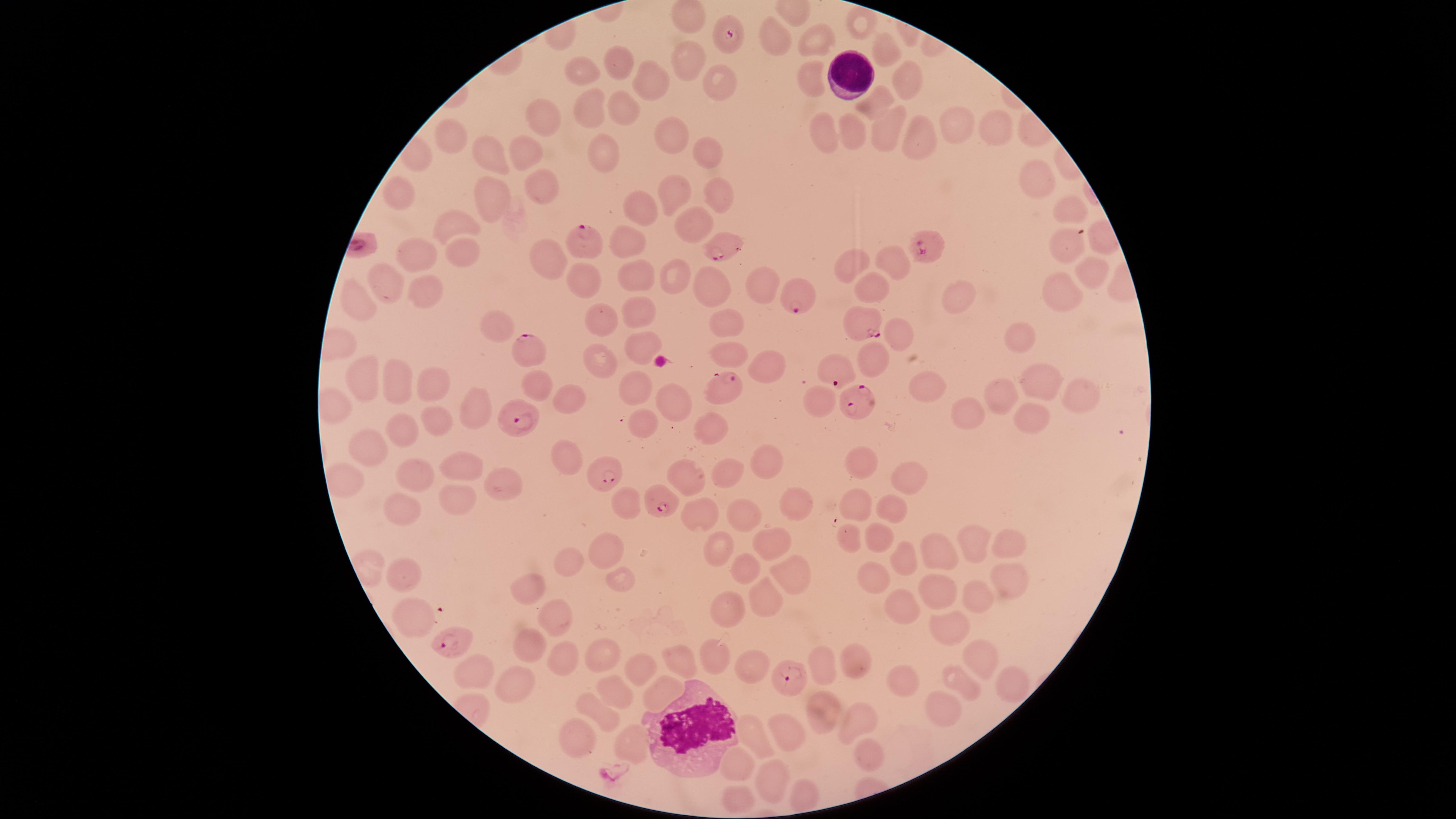
visible region = circular
preparation = thin smear of blood
species = Plasmodium falciparum
uninfected RBCs = approximate marker points, in pixels from the top-left corner: (x=862, y=21), (x=773, y=35), (x=810, y=36), (x=885, y=47), (x=687, y=52), (x=617, y=64), (x=586, y=73), (x=904, y=76), (x=810, y=79), (x=715, y=81), (x=655, y=84), (x=881, y=101), (x=620, y=106), (x=587, y=110), (x=541, y=122), (x=957, y=122), (x=885, y=124), (x=992, y=127), (x=915, y=132), (x=822, y=133), (x=854, y=134), (x=452, y=136), (x=673, y=137), (x=704, y=149), (x=494, y=153), (x=527, y=155), (x=602, y=158), (x=1033, y=178), (x=541, y=182), (x=677, y=189), (x=722, y=191), (x=399, y=197), (x=492, y=197), (x=640, y=209), (x=1068, y=209), (x=696, y=222), (x=449, y=224), (x=629, y=242), (x=1067, y=243), (x=459, y=256), (x=414, y=258), (x=891, y=260), (x=543, y=265), (x=850, y=267), (x=1091, y=272), (x=584, y=276), (x=636, y=277), (x=675, y=277), (x=707, y=285), (x=388, y=287), (x=759, y=287), (x=876, y=289), (x=1064, y=290), (x=427, y=293), (x=959, y=296), (x=360, y=301), (x=634, y=314), (x=605, y=323), (x=1026, y=328), (x=729, y=329), (x=499, y=330), (x=897, y=333), (x=642, y=345), (x=733, y=353), (x=602, y=357), (x=871, y=363), (x=765, y=367), (x=361, y=376), (x=429, y=382), (x=394, y=385), (x=536, y=386), (x=1037, y=386), (x=637, y=388), (x=1078, y=390), (x=567, y=392), (x=931, y=392), (x=1001, y=395), (x=675, y=402), (x=822, y=402), (x=1031, y=407), (x=470, y=408), (x=972, y=412), (x=439, y=416), (x=642, y=419), (x=402, y=421), (x=710, y=422), (x=373, y=452), (x=562, y=457), (x=864, y=458), (x=467, y=459), (x=764, y=465), (x=418, y=471), (x=681, y=473), (x=724, y=476), (x=906, y=480), (x=502, y=486), (x=459, y=499), (x=792, y=504), (x=624, y=505), (x=857, y=505), (x=887, y=511), (x=404, y=512), (x=705, y=513), (x=748, y=517), (x=851, y=536), (x=876, y=536), (x=973, y=546), (x=765, y=547), (x=1009, y=549), (x=602, y=553), (x=716, y=554), (x=939, y=555), (x=900, y=556), (x=568, y=563), (x=873, y=566), (x=748, y=567), (x=404, y=573), (x=785, y=574), (x=616, y=579), (x=1008, y=583), (x=526, y=586), (x=936, y=590), (x=765, y=594), (x=976, y=597), (x=901, y=609), (x=730, y=610), (x=414, y=611), (x=557, y=616), (x=951, y=628), (x=527, y=641), (x=711, y=653), (x=602, y=656), (x=970, y=656), (x=559, y=657), (x=679, y=658), (x=821, y=662), (x=745, y=665), (x=859, y=665), (x=645, y=669), (x=473, y=672), (x=893, y=681), (x=962, y=682), (x=1005, y=682), (x=516, y=685), (x=664, y=693), (x=613, y=694), (x=941, y=708), (x=820, y=709), (x=600, y=713), (x=859, y=722), (x=784, y=730), (x=576, y=736), (x=753, y=737), (x=635, y=739), (x=867, y=753), (x=741, y=762), (x=776, y=782)
parasitized RBCs = approximate marker points, in pixels from the top-left corner: (x=727, y=32), (x=587, y=241), (x=723, y=248), (x=928, y=249), (x=801, y=299), (x=864, y=326), (x=530, y=349), (x=833, y=371), (x=721, y=387), (x=856, y=402), (x=524, y=422), (x=606, y=480), (x=664, y=508), (x=454, y=642), (x=789, y=675)
stain = Giemsa
WBCs = approximate marker points, in pixels from the top-left corner: (x=849, y=72), (x=687, y=728)
presence = malaria parasites seen
field of view = single
image size = 1456×819 pixels
capture = smartphone photograph through the microscope eyepiece